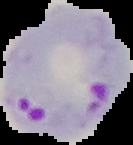
{
  "preparation": "thin blood film",
  "result": "malaria parasites identified",
  "image_size": "133×145 pixels",
  "image_type": "segmented cell region with the area outside set to black"
}